Evaluate for malaria.
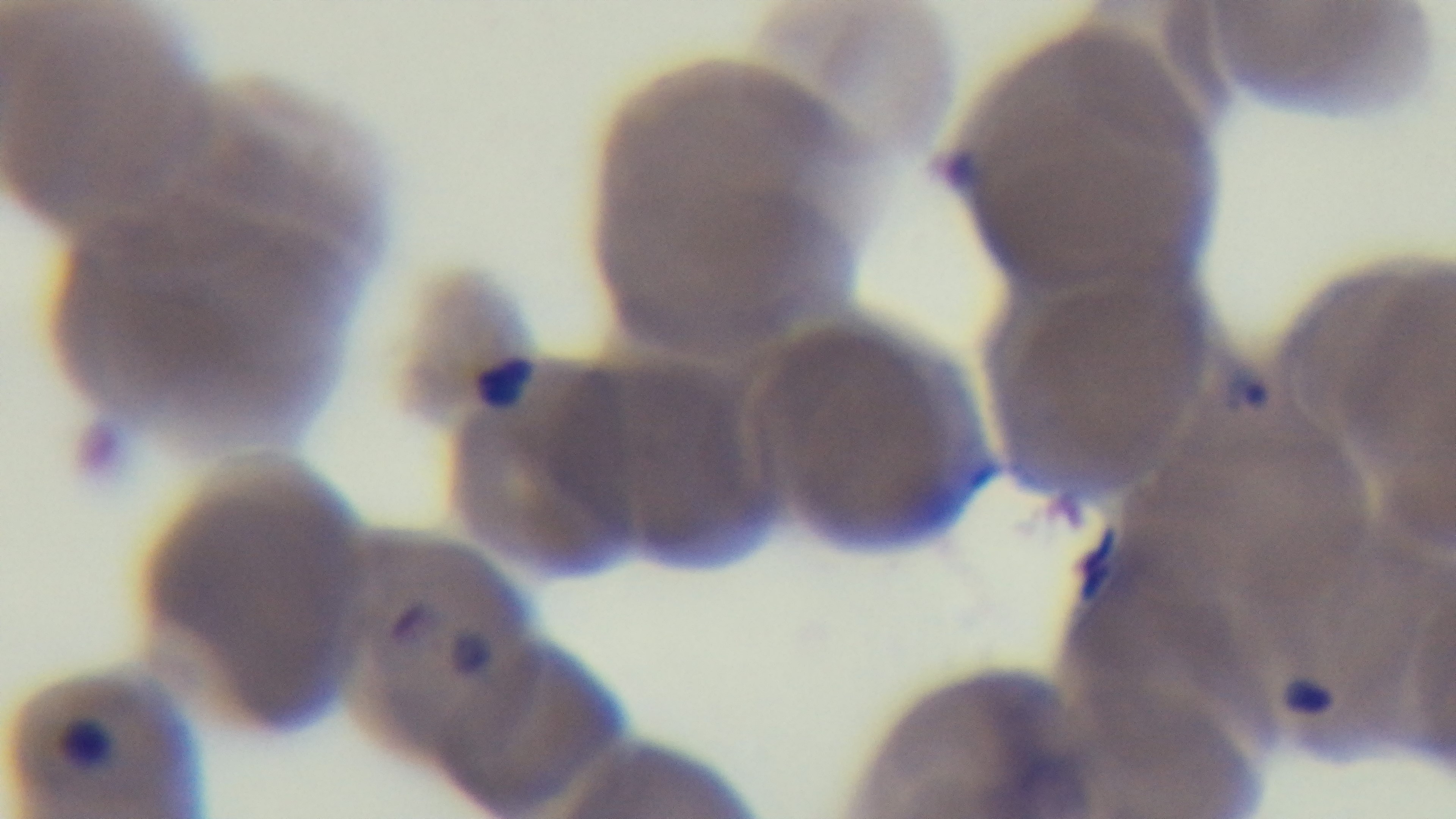

Positive.

capture = mounted 4K digital camera
objective = 100x oil immersion
field of view = one from the slide
modality = light microscopy
preparation = thin
stain = Giemsa